Describe the morphology of the erythrocytes.
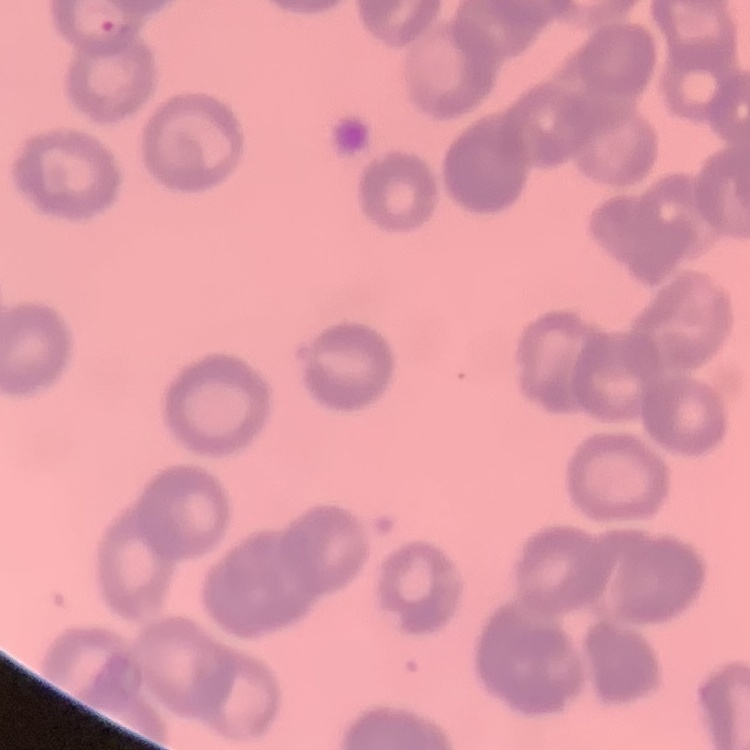

They show rouleaux formation.

Summary:
  - Image type: square crop of a larger photomicrograph
  - Stain: Field's or Giemsa
  - Preparation: thin blood smear